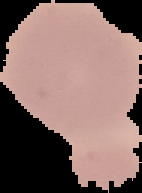

{
  "preparation": "thin blood smear",
  "image_size": "142×193 pixels",
  "image_type": "segmented cell region with the area outside set to black",
  "result": "no malaria parasites detected"
}